Name the parasite shown.
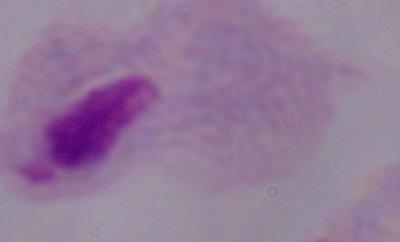
This is a trichomonad.

Captured at 1000x magnification. Micrograph.